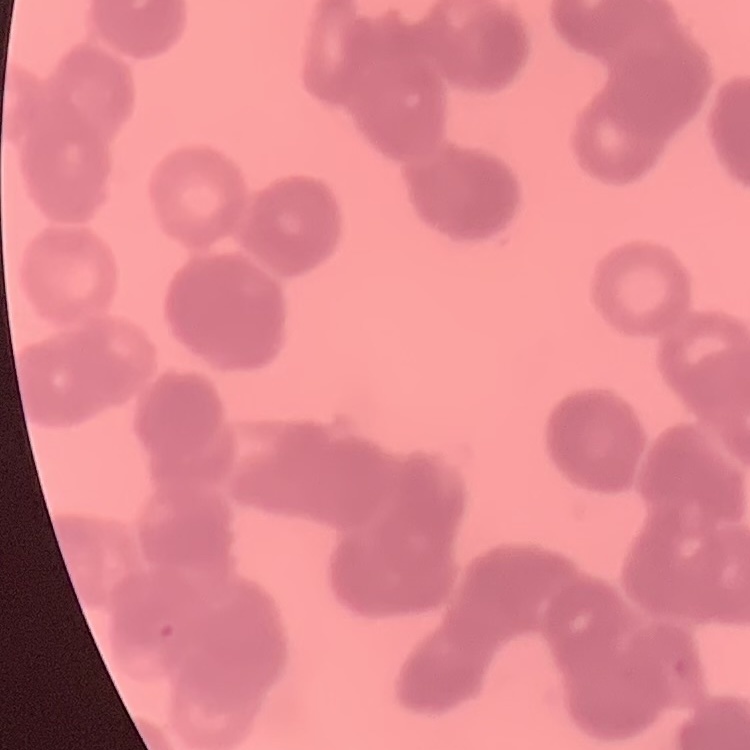

Summary:
  - Red blood cell morphology: rouleaux formation
  - Image type: one tile cut from a larger photomicrograph
  - Stain: Field's or Giemsa
  - Preparation: thin blood smear